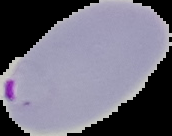
From a thin blood smear. Image is 172×136 pixels. Result: Plasmodium parasites detected. Segmented cell region on a black background.